Comment on the morphology of the red blood cells.
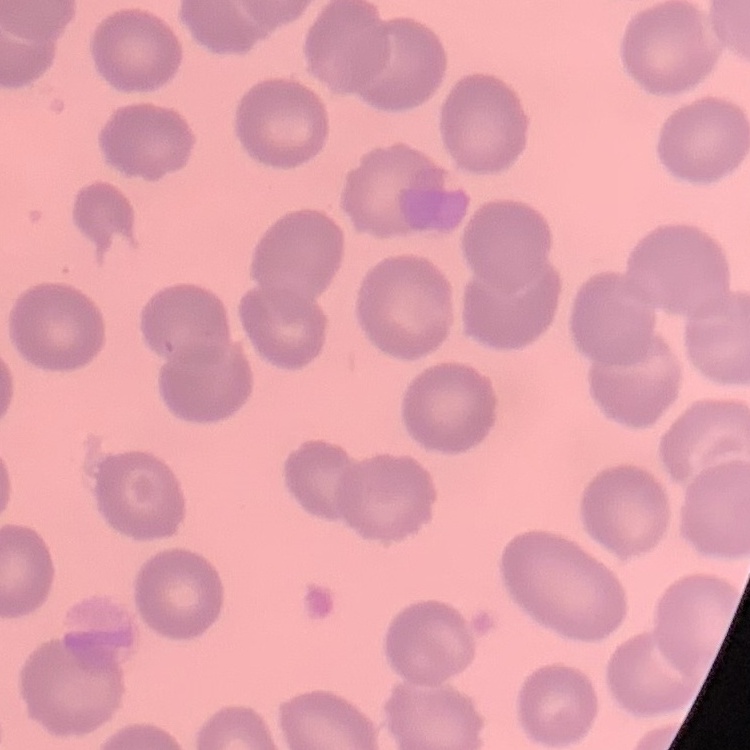
No rouleaux formation.

image type = one tile cut from a larger photomicrograph
preparation = thin blood smear
stain = Field's or Giemsa